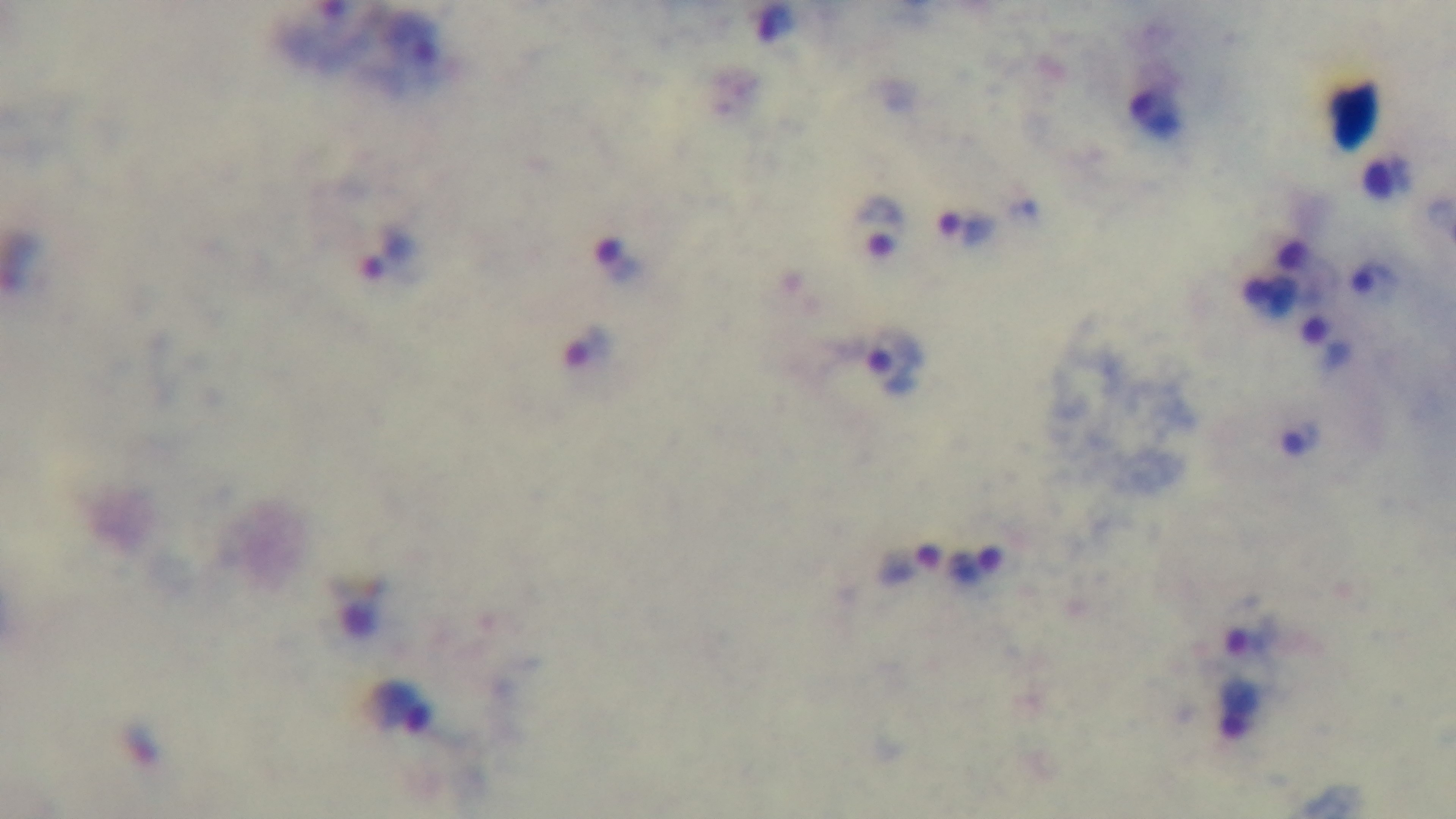
Summary:
  - Modality: light microscopy
  - Capture: mounted 4K digital camera
  - Stain: Giemsa
  - Field of view: single
  - Preparation: thick
  - Objective: 100x oil immersion
  - Malaria status: positive